Assess this cell for malaria.
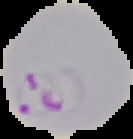

Parasitized.

{
  "preparation": "thin blood film",
  "image_type": "segmented cell region with the area outside set to black",
  "image_size": "133×139 pixels"
}